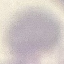 Malaria status: uninfected. Acquired by smartphone through the microscope eyepiece. Giemsa-stained preparation. Thin blood film. Cell patch, automatically extracted from a larger field of view and resized to 64 × 64 pixels.